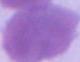

identification = red blood cell
modality = micrograph
magnification = 1000x